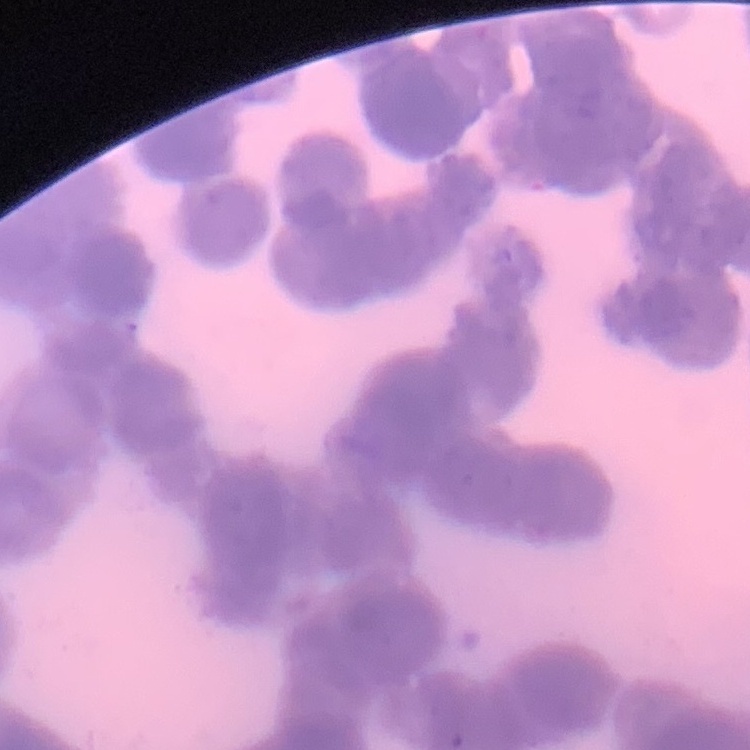

Summary:
  - Erythrocyte morphology: rouleaux formation
  - Image type: one tile cut from a larger photomicrograph
  - Preparation: thin blood film
  - Stain: Field's or Giemsa